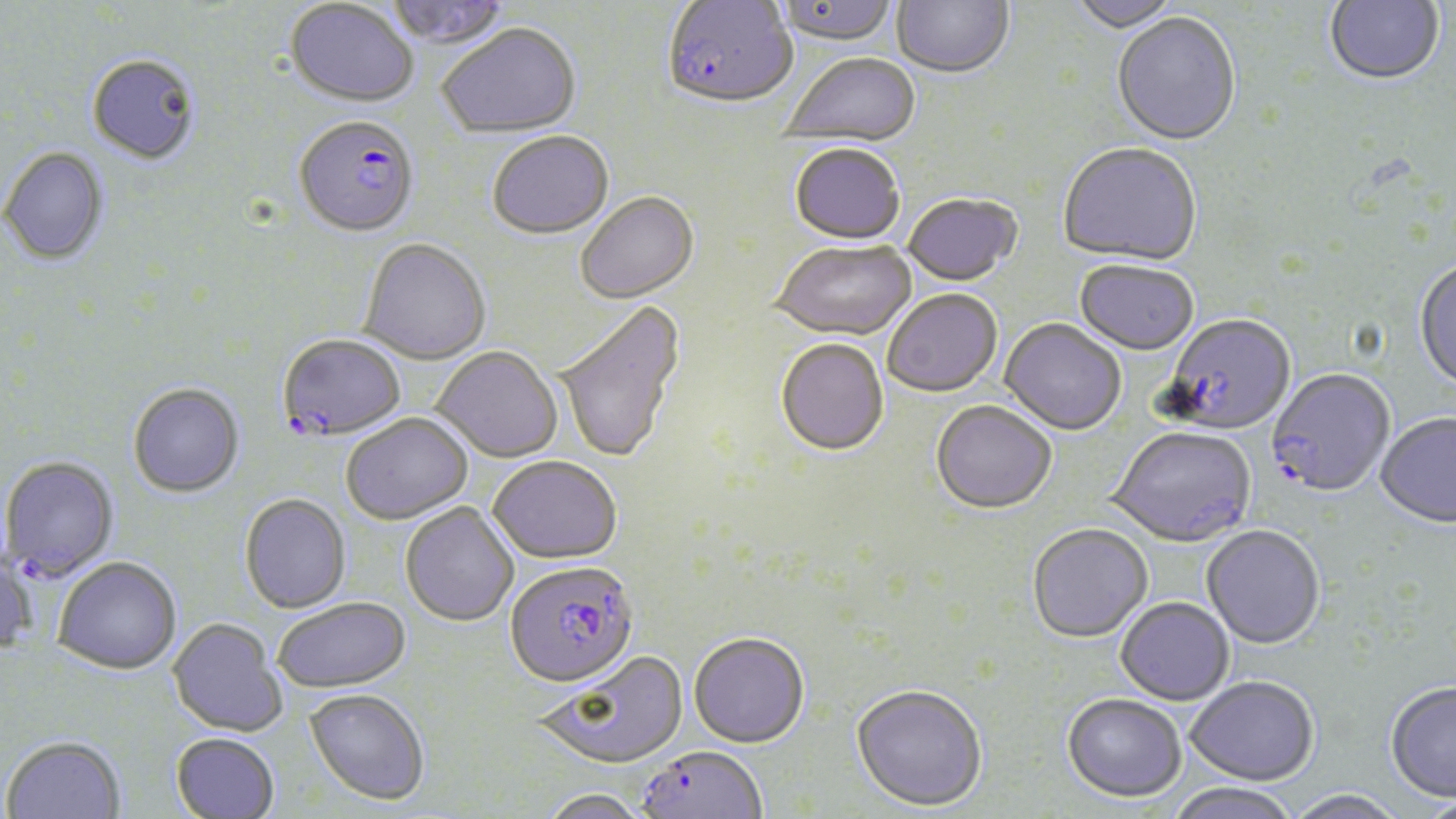 Approximate bounding boxes as named x1/y1/x2/y2 corners in pixels. Uninfected red blood cell locations: (x1=383, y1=0, x2=510, y2=51), (x1=891, y1=0, x2=1014, y2=82), (x1=1067, y1=0, x2=1185, y2=35), (x1=1325, y1=0, x2=1444, y2=87), (x1=285, y1=1, x2=418, y2=108), (x1=773, y1=1, x2=900, y2=50), (x1=1112, y1=15, x2=1242, y2=148), (x1=437, y1=25, x2=582, y2=140), (x1=86, y1=54, x2=200, y2=164), (x1=781, y1=54, x2=922, y2=149), (x1=487, y1=133, x2=614, y2=242), (x1=1058, y1=144, x2=1202, y2=268), (x1=789, y1=146, x2=905, y2=247), (x1=1, y1=148, x2=110, y2=267), (x1=575, y1=194, x2=700, y2=306), (x1=901, y1=195, x2=1022, y2=289), (x1=359, y1=240, x2=491, y2=366), (x1=770, y1=242, x2=918, y2=343), (x1=1414, y1=260, x2=1456, y2=393), (x1=1074, y1=262, x2=1198, y2=358), (x1=883, y1=291, x2=1002, y2=400), (x1=554, y1=300, x2=686, y2=467), (x1=999, y1=320, x2=1126, y2=437), (x1=775, y1=341, x2=889, y2=458), (x1=431, y1=347, x2=563, y2=463), (x1=127, y1=383, x2=245, y2=499), (x1=930, y1=402, x2=1057, y2=516), (x1=341, y1=414, x2=473, y2=525), (x1=1376, y1=414, x2=1456, y2=530), (x1=1107, y1=428, x2=1257, y2=549), (x1=488, y1=457, x2=622, y2=565), (x1=240, y1=493, x2=352, y2=614), (x1=401, y1=503, x2=520, y2=627), (x1=1027, y1=523, x2=1153, y2=643), (x1=1204, y1=523, x2=1327, y2=647), (x1=0, y1=555, x2=37, y2=657), (x1=54, y1=558, x2=182, y2=675), (x1=272, y1=597, x2=410, y2=693), (x1=1115, y1=597, x2=1234, y2=705), (x1=167, y1=618, x2=288, y2=737), (x1=689, y1=632, x2=810, y2=748), (x1=536, y1=652, x2=690, y2=770), (x1=1184, y1=676, x2=1319, y2=785), (x1=1385, y1=680, x2=1456, y2=803), (x1=851, y1=685, x2=988, y2=812), (x1=304, y1=688, x2=430, y2=805), (x1=1062, y1=693, x2=1187, y2=802), (x1=170, y1=732, x2=280, y2=818), (x1=2, y1=737, x2=125, y2=819), (x1=1164, y1=782, x2=1302, y2=819), (x1=537, y1=788, x2=651, y2=819), (x1=1282, y1=789, x2=1409, y2=819). Plasmodium falciparum-infected red blood cell locations: (x1=661, y1=1, x2=798, y2=113), (x1=294, y1=116, x2=419, y2=239), (x1=1161, y1=316, x2=1295, y2=437), (x1=276, y1=334, x2=406, y2=442), (x1=1266, y1=370, x2=1395, y2=499), (x1=1, y1=457, x2=119, y2=582), (x1=505, y1=563, x2=639, y2=692), (x1=636, y1=746, x2=768, y2=819). Slide-level diagnosis: Plasmodium falciparum. Captured at 1000x magnification. Light microscopy. May-Grünwald-Giemsa stain. Image is 1456×819 pixels. Thin blood film. Single field of view.